Name the parasite shown.
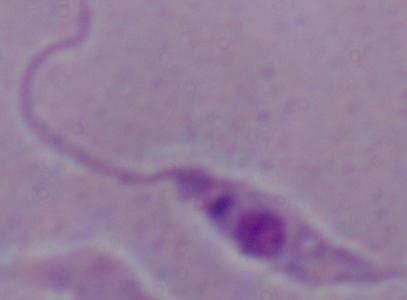
Leishmania.

{
  "modality": "micrograph",
  "magnification": "1000x"
}